Locate every Plasmodium parasite.
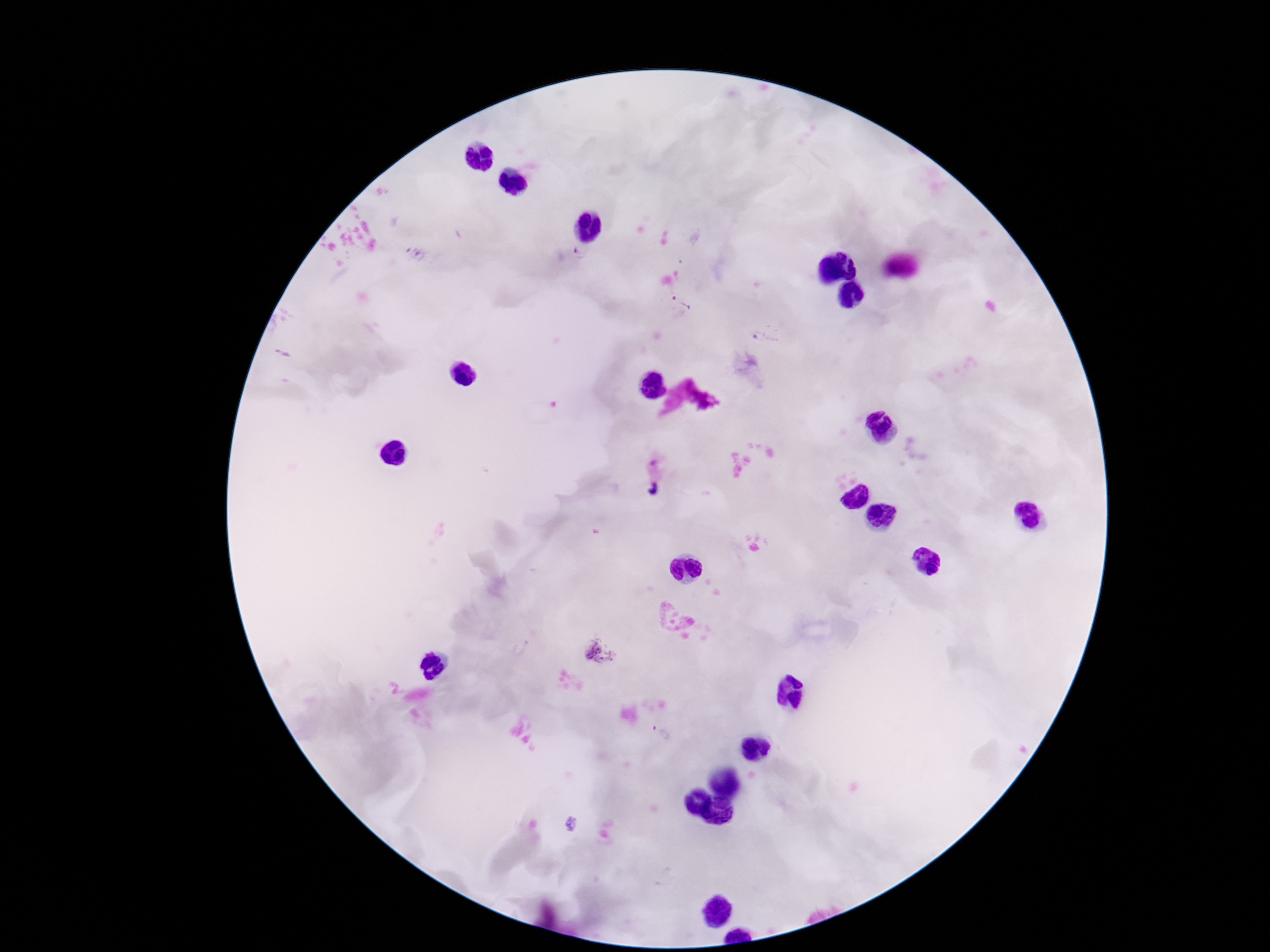

Approximate centers as (x, y) in pixels.
Plasmodium parasites: (415, 253), (580, 253), (682, 305), (765, 339), (601, 651).

Smartphone photograph taken through the microscope eyepiece. Image is 1270×952 pixels. 100x magnification. Giemsa stain. Thick peripheral-blood smear. Patient malaria status: infected. Single field of view.